Locate every malaria parasite.
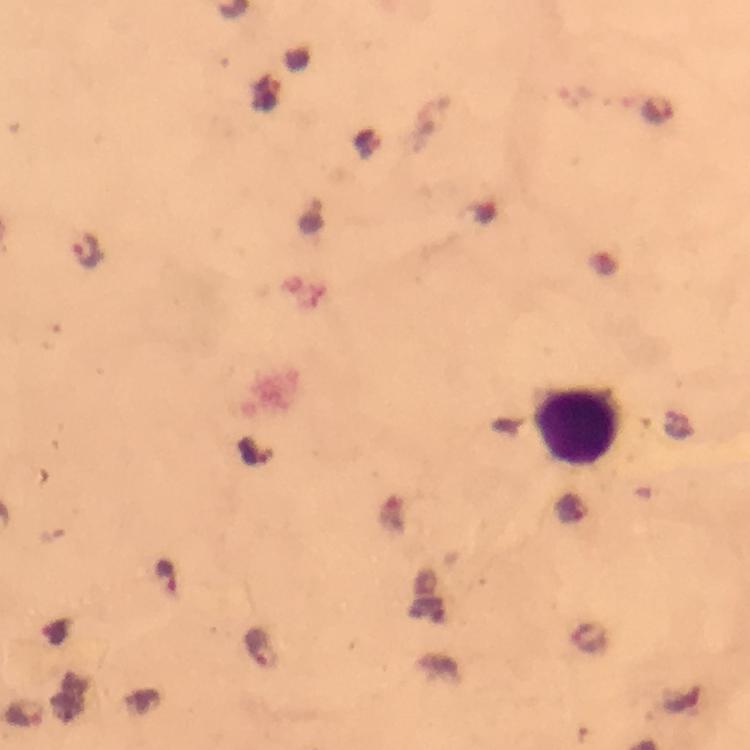
Approximate object centers, in pixels from the top-left corner.
Malaria parasites: (x=657, y=108), (x=87, y=251), (x=254, y=453), (x=571, y=511), (x=164, y=575), (x=259, y=648).

Leukocyte locations: (x=575, y=422). Immersion oil was used. From a diagnostic examination for malaria. Cropped region of a single field of view. Giemsa-stained preparation. 100x magnification. Image is 750×750 pixels. Thick blood smear. Photographed with a smartphone mounted on the microscope.